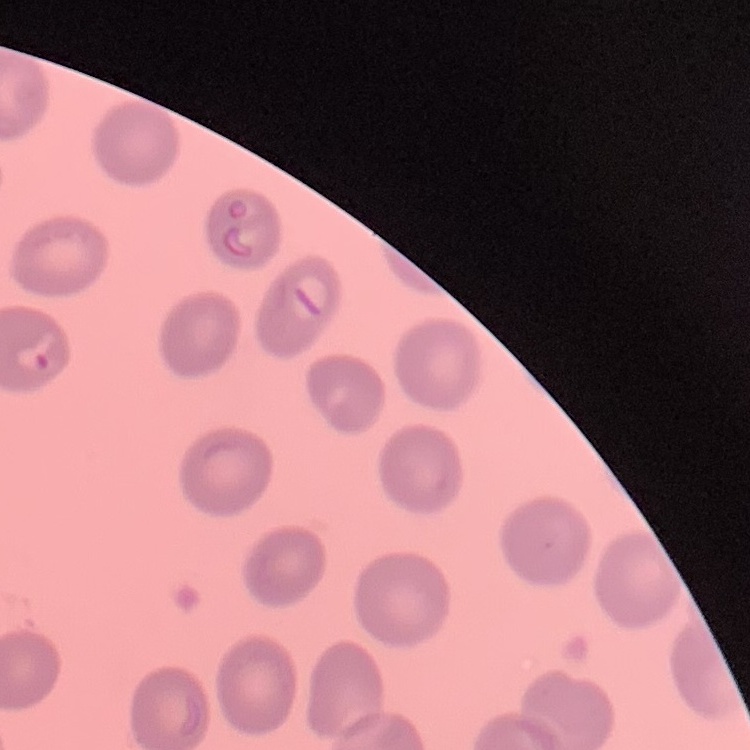
Summary:
  - Red blood cell morphology: no rouleaux formation
  - Image type: square crop of a larger photomicrograph
  - Stain: Field's or Giemsa
  - Preparation: thin peripheral smear